Evaluate for parasitized red blood cells.
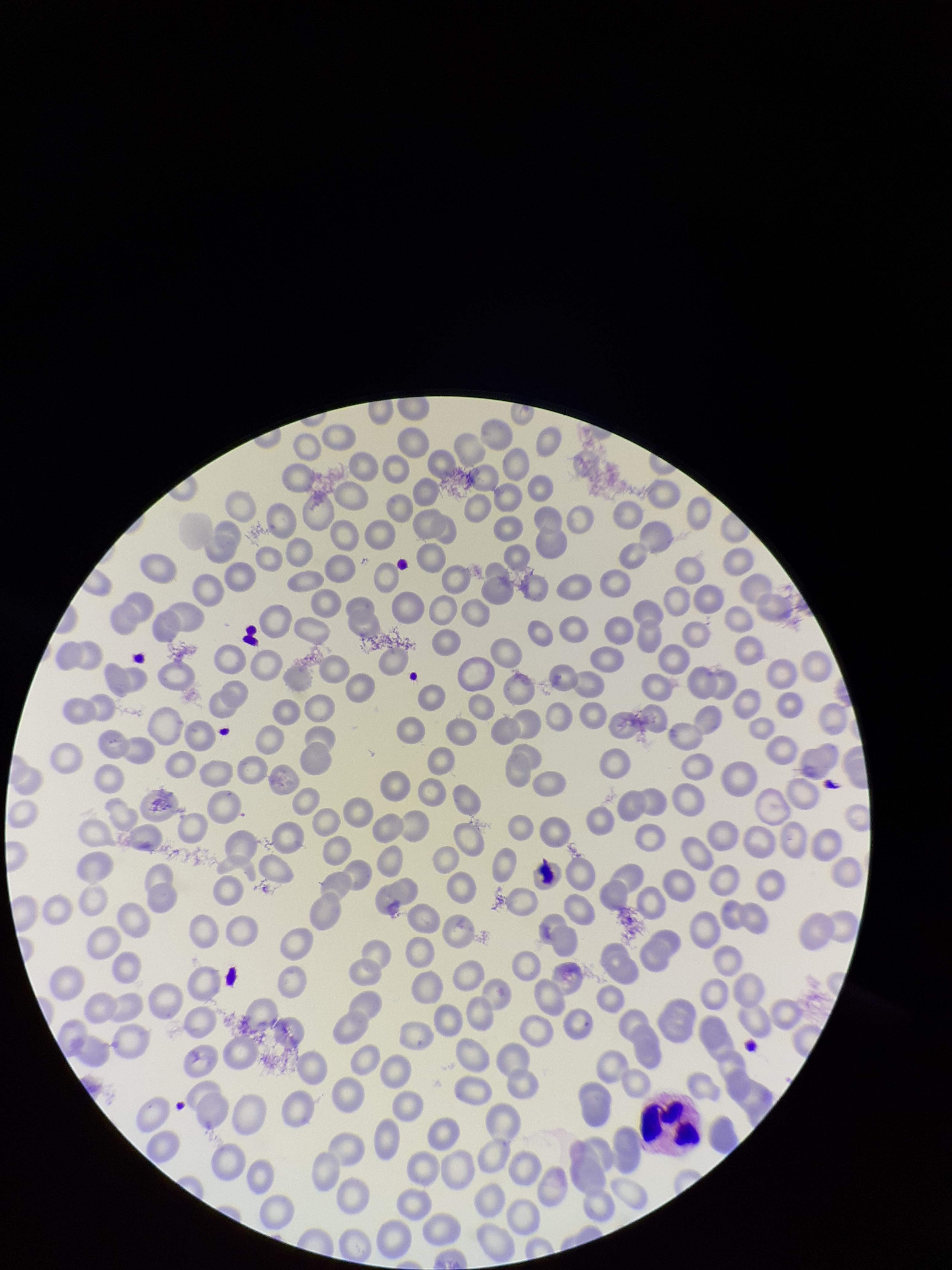
None identified.

field of view = single
stain = Giemsa
red blood cell count = 274
capture = smartphone photograph through the microscope eyepiece
patient malaria status = negative
parasitized red blood cell count = 0
preparation = thin smear
image size = 952×1270 pixels